Name the parasite shown.
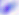

This is Toxoplasma gondii.

400x magnification. Micrograph.